Locate and identify every blood parasite.
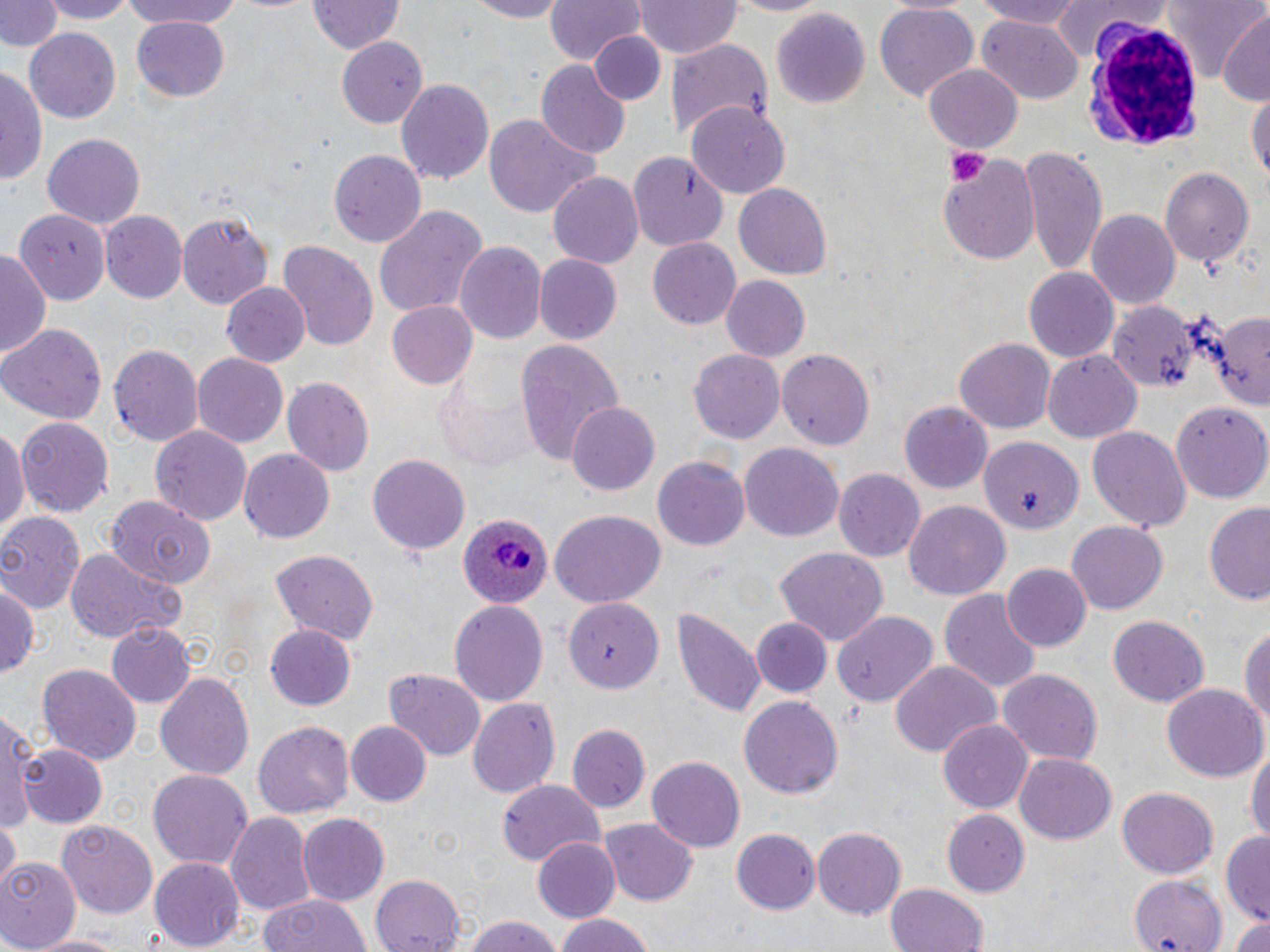
Approximate bounding boxes as [x1, y1, x2, y2] in pixels.
Plasmodium ovale-infected red blood cells: [457, 512, 554, 609].
No Plasmodium falciparum, Plasmodium malariae, Plasmodium vivax, Babesia divergens, or Trypanosoma brucei observed.

Platelet locations: [945, 147, 992, 187]. Uninfected red blood cell locations: [2, 0, 61, 55], [33, 0, 141, 23], [112, 0, 254, 29], [460, 0, 573, 21], [544, 0, 642, 67], [634, 0, 742, 59], [969, 0, 1088, 27], [1163, 0, 1266, 86], [309, 1, 404, 55], [1046, 2, 1171, 60], [873, 3, 979, 103], [768, 7, 870, 108], [1214, 14, 1269, 105], [133, 17, 230, 101], [979, 18, 1083, 103], [24, 28, 121, 124], [589, 31, 666, 106], [336, 37, 428, 126], [666, 40, 776, 141], [536, 60, 630, 161], [0, 61, 46, 191], [925, 64, 1022, 153], [395, 78, 496, 184], [1247, 86, 1269, 191], [686, 101, 790, 197], [482, 115, 599, 219], [42, 132, 147, 228], [1019, 145, 1106, 273], [630, 148, 731, 252], [328, 149, 426, 248], [936, 152, 1041, 262], [1160, 166, 1257, 267], [548, 171, 643, 271], [735, 184, 832, 280], [374, 205, 488, 319], [13, 207, 110, 303], [1087, 210, 1181, 312], [100, 212, 186, 301], [177, 212, 274, 308], [279, 238, 379, 353], [646, 238, 741, 330], [455, 243, 546, 346], [0, 247, 50, 358], [534, 254, 622, 344], [1024, 267, 1118, 363], [721, 275, 811, 363], [221, 283, 309, 368], [388, 301, 479, 389], [1106, 301, 1198, 389], [1197, 305, 1270, 416], [0, 323, 108, 424], [513, 338, 625, 466], [956, 338, 1055, 432], [108, 341, 205, 447], [689, 348, 785, 444], [776, 348, 877, 451], [192, 353, 288, 447], [1044, 353, 1141, 441], [435, 375, 540, 472], [282, 377, 374, 477], [1171, 398, 1270, 503], [899, 401, 993, 494], [568, 402, 658, 495], [16, 416, 115, 517], [0, 425, 29, 542], [151, 426, 251, 524], [1087, 426, 1190, 531], [974, 431, 1086, 537], [740, 444, 844, 540], [238, 448, 335, 543], [368, 452, 470, 555], [654, 455, 750, 553], [834, 469, 926, 563], [105, 498, 216, 589], [1202, 498, 1270, 608], [905, 502, 1011, 602], [549, 509, 664, 608], [0, 513, 84, 614], [1067, 521, 1167, 615], [773, 546, 888, 646], [65, 547, 176, 643], [269, 547, 379, 642], [1001, 563, 1091, 652], [0, 576, 39, 685], [941, 588, 1041, 695], [450, 598, 548, 705], [563, 599, 661, 695], [671, 604, 764, 720], [830, 609, 937, 709], [749, 614, 833, 699], [1106, 614, 1209, 707], [105, 621, 195, 710], [1240, 623, 1270, 738], [266, 624, 356, 710], [36, 661, 141, 762], [891, 661, 999, 762], [997, 668, 1103, 766], [153, 670, 255, 783], [386, 670, 485, 759], [1162, 683, 1266, 782], [739, 695, 844, 799], [467, 697, 561, 799], [2, 712, 39, 831], [939, 718, 1034, 815], [254, 720, 353, 818], [345, 720, 431, 806], [568, 724, 651, 813], [1246, 742, 1270, 852], [17, 743, 107, 827], [1015, 754, 1117, 845], [647, 757, 747, 852], [149, 768, 253, 869], [496, 780, 605, 865], [1117, 787, 1217, 877], [941, 809, 1029, 896], [226, 812, 316, 918], [296, 812, 389, 906], [0, 818, 20, 887], [600, 818, 697, 906], [56, 820, 156, 921], [813, 826, 907, 918], [730, 830, 818, 916], [1219, 830, 1270, 925], [280, 835, 384, 947], [532, 836, 620, 923], [0, 857, 78, 950], [150, 857, 245, 950], [370, 873, 467, 952], [1130, 874, 1228, 952], [886, 882, 989, 952], [257, 893, 371, 952], [1226, 911, 1270, 952], [552, 912, 660, 952], [465, 915, 565, 952], [28, 932, 126, 952]. White blood cell locations: [1088, 18, 1199, 147]. Slide-level diagnosis: Plasmodium ovale. Image is 1270×952 pixels. Thin blood smear. One field of a larger specimen. May-Grünwald-Giemsa stain. 1000x magnification. Light microscopy.